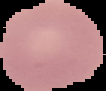
Summary:
  - Image size: 106×91 pixels
  - Result: no malaria parasites seen
  - Image type: segmented cell region with the area outside set to black
  - Preparation: thin blood film